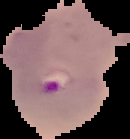

Result: Plasmodium parasites identified. From a thin blood smear. Segmented cell region on a black background. Image is 130×139 pixels.